Comment on the morphology of the erythrocytes.
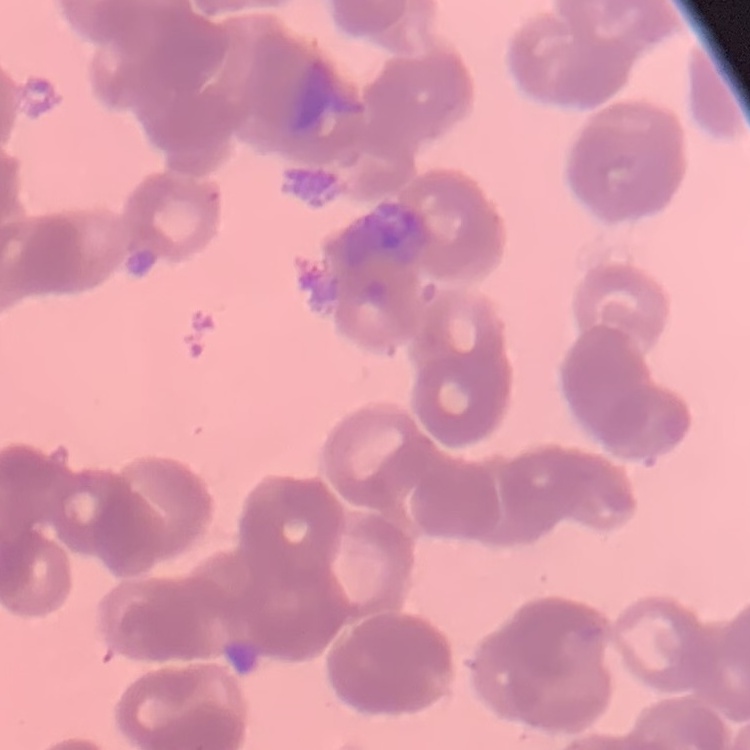
They show rouleaux formation.

stain = Field's or Giemsa
preparation = thin blood smear
image type = one tile cut from a larger photomicrograph